Comment on the morphology of the red blood cells.
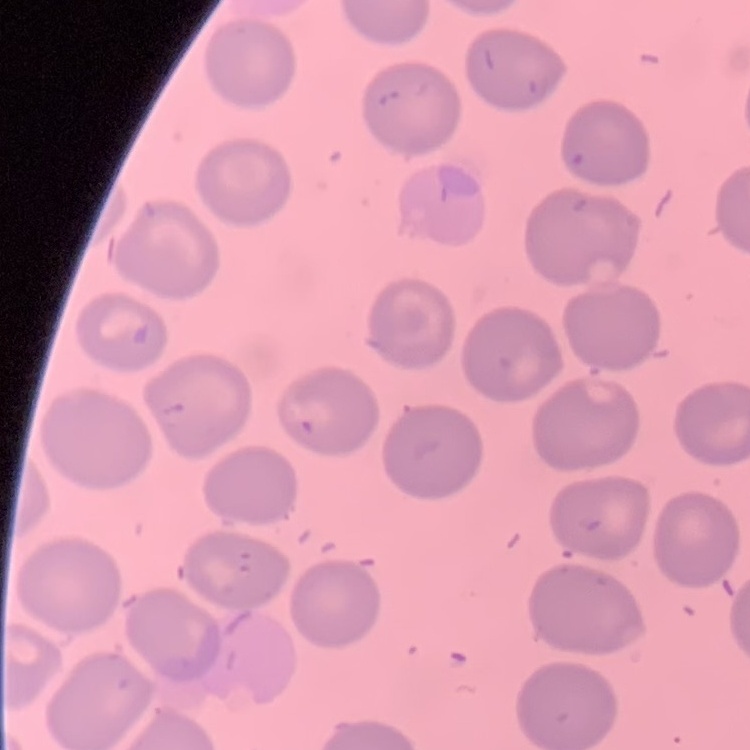
They show no rouleaux formation.

image type = one tile cut from a larger photomicrograph
stain = Field's or Giemsa
preparation = thin peripheral smear